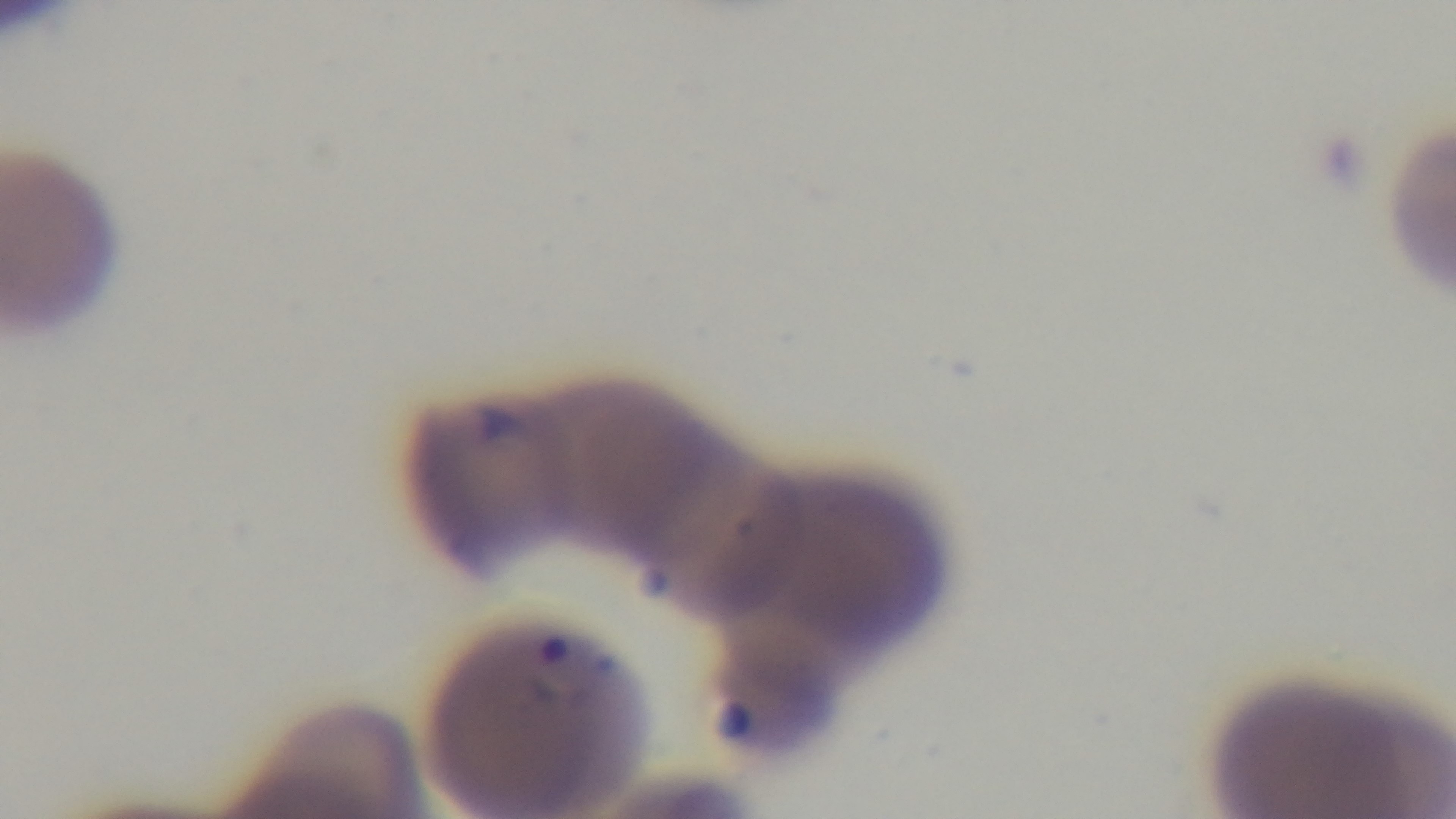 Malaria status: positive. Single field of view. Photomicrograph. Giemsa stain. Captured with a mounted 4K digital camera. Oil-immersion objective, 100x. Preparation: thin blood film.